Locate every blood parasite and identify its species.
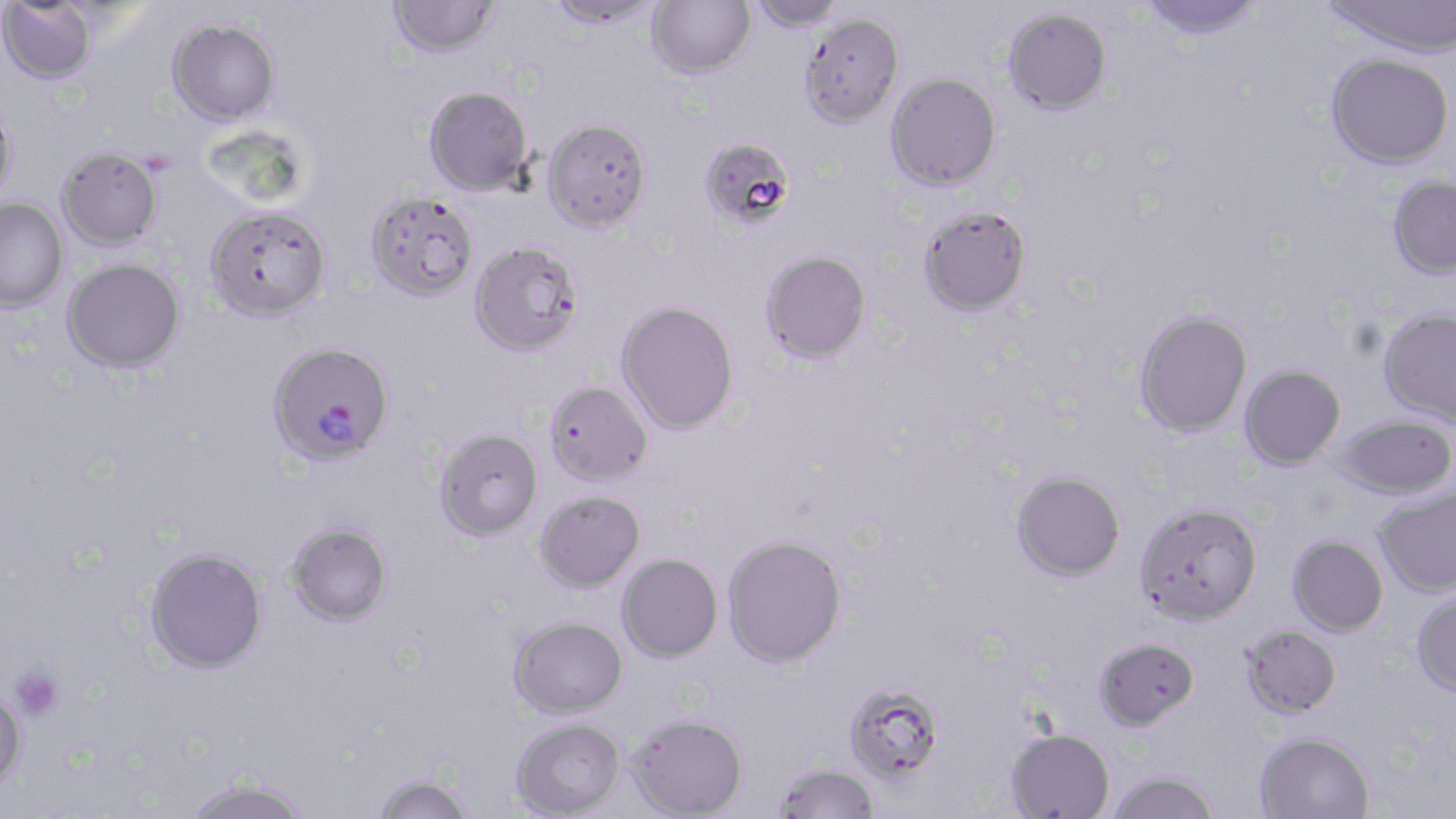

Approximate bounding boxes as (x1, y1, x2, y2) in pixels.
Plasmodium falciparum-infected red blood cells: (267, 344, 394, 470).
No Plasmodium ovale, Plasmodium malariae, Plasmodium vivax, Babesia divergens, or Trypanosoma brucei observed.

Uninfected red blood cell locations: (544, 0, 662, 28), (647, 0, 755, 78), (747, 0, 848, 33), (1139, 0, 1264, 42), (1322, 0, 1455, 59), (386, 1, 501, 58), (0, 2, 99, 85), (1003, 7, 1112, 114), (799, 12, 904, 128), (166, 18, 281, 127), (1326, 52, 1453, 169), (886, 72, 1001, 190), (423, 85, 533, 195), (0, 99, 18, 210), (542, 118, 652, 233), (704, 144, 796, 230), (56, 147, 162, 251), (1387, 175, 1456, 280), (365, 192, 479, 302), (0, 199, 68, 313), (206, 206, 331, 323), (919, 206, 1032, 317), (470, 242, 584, 358), (760, 251, 871, 365), (62, 258, 185, 375), (615, 302, 740, 436), (1377, 308, 1456, 426), (1134, 310, 1252, 437), (1239, 365, 1346, 471), (543, 382, 653, 488), (1332, 414, 1456, 499), (435, 430, 543, 543), (1010, 471, 1126, 582), (1374, 486, 1456, 597), (534, 491, 645, 593), (1134, 502, 1263, 626), (286, 524, 393, 629), (1287, 535, 1388, 636), (722, 536, 847, 669), (145, 549, 268, 675), (617, 553, 723, 664), (1410, 589, 1456, 697), (509, 616, 628, 720), (1240, 625, 1342, 719), (1093, 637, 1200, 731), (844, 683, 945, 785), (0, 689, 27, 799), (626, 714, 748, 819), (511, 719, 626, 818), (1005, 728, 1115, 819), (1254, 731, 1374, 819), (774, 763, 881, 819), (1103, 771, 1221, 818), (372, 773, 474, 819), (183, 779, 312, 819). Platelet locations: (8, 664, 65, 721). Slide-level diagnosis: Plasmodium falciparum. Captured at 1000x magnification. One field of a larger specimen. May-Grünwald-Giemsa-stained preparation. Optical microscopy. Image is 1456×819 pixels. Thin blood smear.